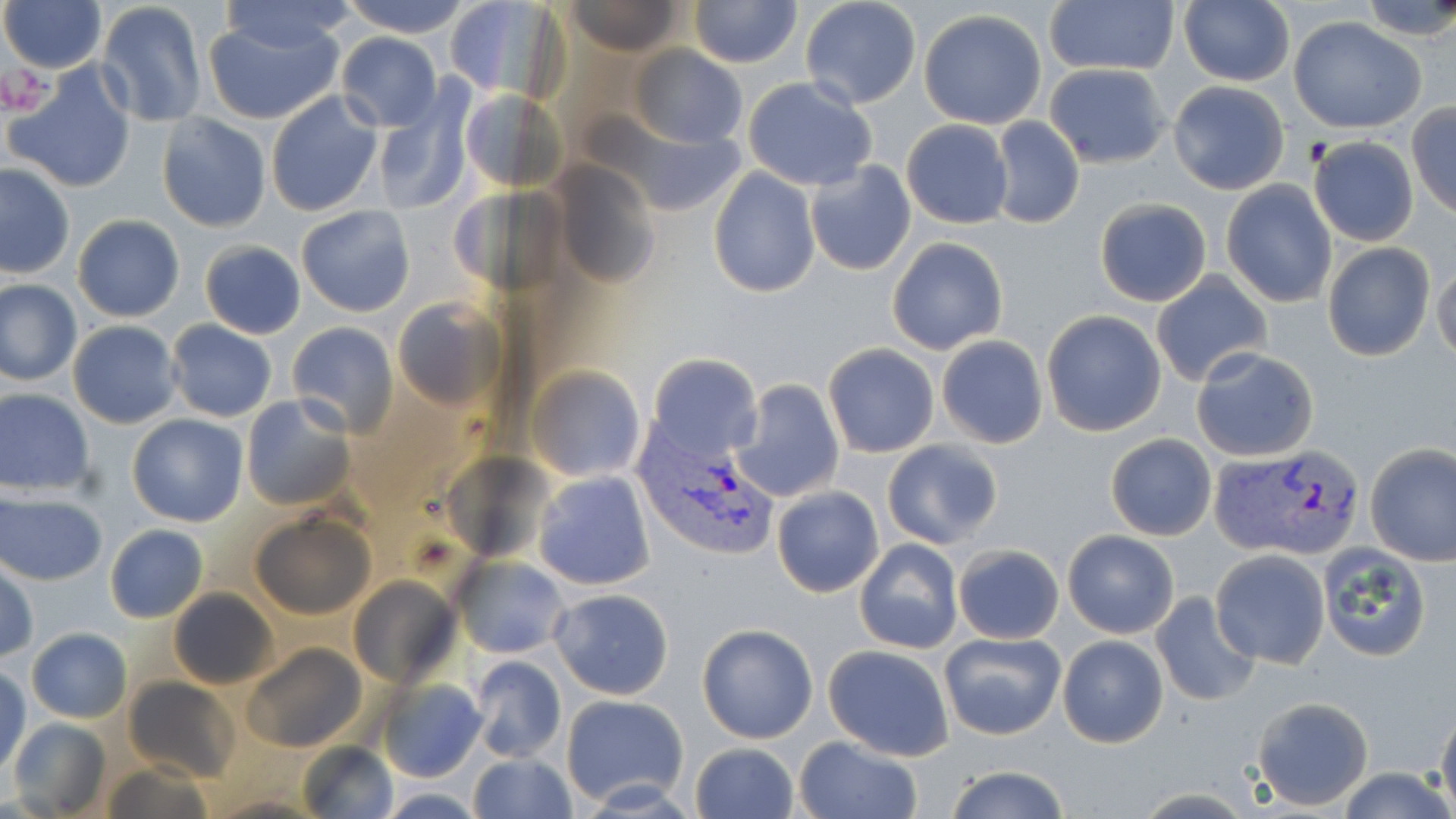 Approximate bounding boxes as (x1,y1)-(x2,y2) corner pairs in pixels. Uninfected red blood cell locations: (1,0)-(107,73), (214,0)-(354,56), (339,0)-(471,37), (444,0)-(559,101), (566,0)-(689,56), (688,0)-(800,68), (800,0)-(921,110), (1357,0)-(1456,44), (97,1)-(207,128), (1044,1)-(1179,77), (1178,1)-(1294,87), (919,9)-(1048,128), (204,16)-(341,125), (1288,17)-(1426,132), (335,33)-(442,130), (627,45)-(748,148), (7,63)-(138,194), (1044,63)-(1170,168), (742,78)-(878,189), (1168,81)-(1290,195), (372,88)-(475,217), (460,89)-(566,189), (266,90)-(383,217), (1406,106)-(1456,218), (156,113)-(271,233), (989,116)-(1084,232), (901,120)-(1014,229), (622,126)-(743,218), (1309,136)-(1419,245), (549,159)-(661,286), (805,159)-(917,276), (0,161)-(74,279), (708,166)-(820,297), (1221,180)-(1337,308), (448,185)-(575,300), (1093,197)-(1212,306), (295,205)-(416,317), (73,213)-(185,322), (886,236)-(1008,355), (200,240)-(305,339), (1321,243)-(1435,360), (1432,257)-(1456,365), (1151,271)-(1272,387), (0,280)-(82,385), (392,298)-(505,412), (1041,310)-(1166,437), (69,319)-(180,427), (166,320)-(277,421), (287,321)-(398,435), (936,335)-(1048,449), (823,343)-(939,457), (1192,346)-(1319,462), (646,353)-(763,462), (528,366)-(648,481), (731,379)-(846,505), (0,389)-(98,495), (241,395)-(356,510), (127,413)-(248,527), (1105,433)-(1218,541), (880,439)-(1003,549), (1365,444)-(1456,566), (532,471)-(656,591), (771,486)-(884,597), (1,490)-(107,586), (249,512)-(375,620), (104,524)-(208,623), (1061,529)-(1180,639), (854,539)-(963,653), (1319,541)-(1436,660), (951,544)-(1064,643), (1210,550)-(1330,669), (450,555)-(571,659), (1,561)-(37,664), (349,577)-(462,689), (548,588)-(674,699), (169,589)-(278,688), (1150,592)-(1260,706), (695,624)-(817,744), (27,627)-(131,724), (940,633)-(1066,740), (1058,635)-(1169,748), (242,643)-(368,752), (824,644)-(954,759), (468,655)-(567,763), (1,665)-(29,778), (124,677)-(241,781), (378,679)-(486,783), (560,694)-(690,809), (1250,697)-(1374,811), (1436,704)-(1456,814), (10,721)-(111,814), (794,736)-(922,819), (297,741)-(400,819), (689,742)-(799,819), (467,752)-(577,819), (98,760)-(215,819), (942,765)-(1071,819), (1338,767)-(1453,819), (378,787)-(486,818), (203,793)-(333,819). Plasmodium vivax-infected red blood cell locations: (633,426)-(778,563), (1214,445)-(1367,561). Platelet locations: (4,66)-(52,117). Slide-level diagnosis: Plasmodium vivax. Image is 1456×819 pixels. Thin blood film. 1000x magnification. Optical microscopy. May-Grünwald-Giemsa stain. One field of a larger specimen.